Report the malaria status of this cell.
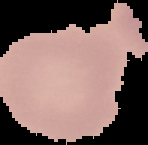
Uninfected.

image type = segmented cell region on a black background
image size = 148×145 pixels
preparation = thin blood smear